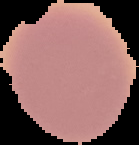
{
  "image_size": "139×145 pixels",
  "malaria_status": "uninfected",
  "image_type": "segmented cell region with the area outside set to black",
  "preparation": "thin blood smear"
}